Point out each Plasmodium parasite and classify it by life-cycle stage.
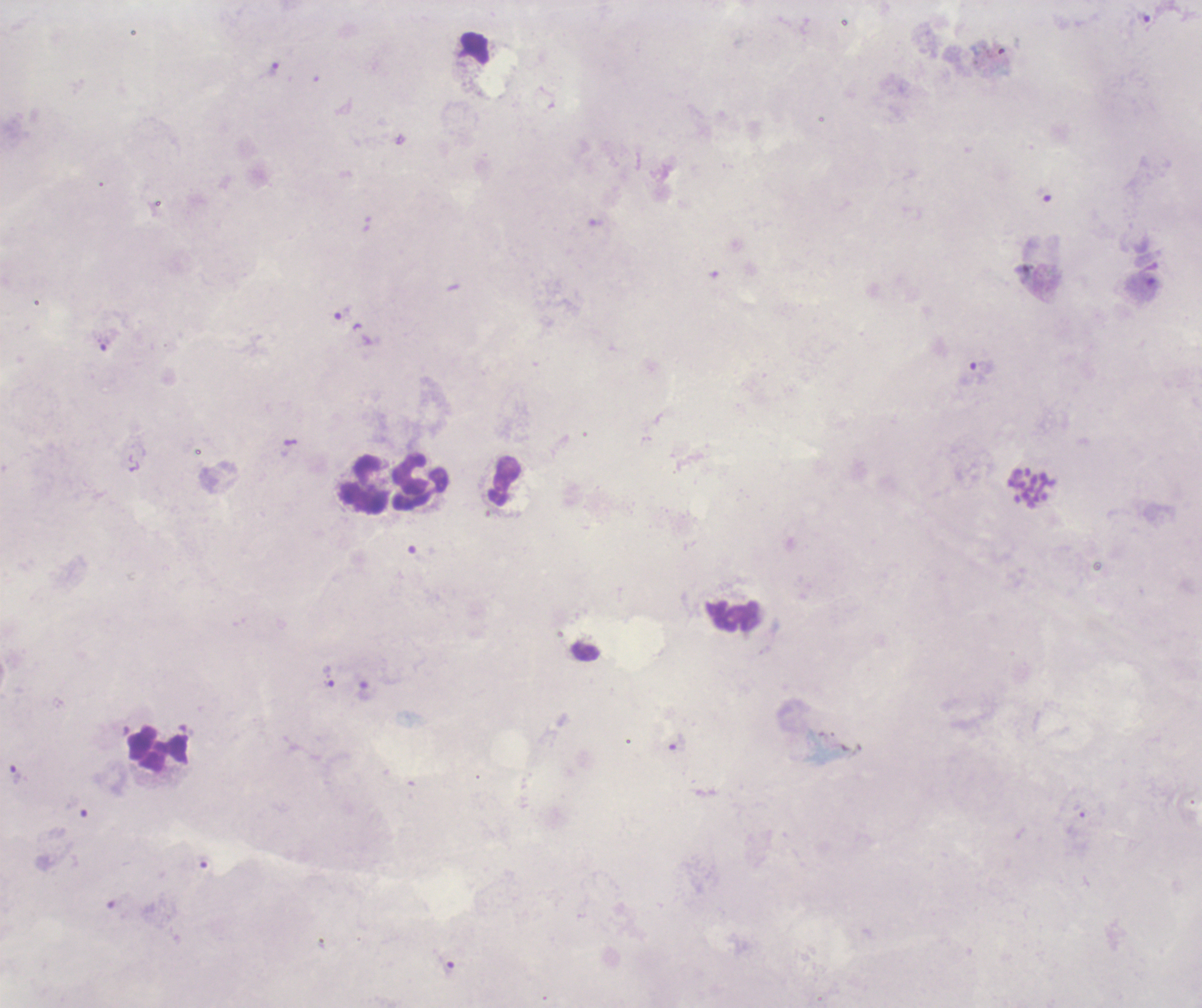
Approximate centers as {x, y} in pixels.
Trophozoites: {1144, 20}, {272, 70}, {342, 313}, {105, 344}, {979, 370}, {330, 681}, {365, 693}, {678, 742}, {16, 775}, {447, 965}.
Schizonts: {1032, 487}.
No gametocyte forms observed.

Approximate centers as {x, y} in pixels.
Summary:
  - Leukocyte locations: {505, 482}, {365, 483}, {420, 483}, {733, 614}, {158, 748}
  - Preparation: thick blood smear
  - Stain: Romanowsky
  - Image size: 1202×1008 pixels
  - Field of view: one from this slide
  - Magnification: 100x
  - Context: previously used in a real diagnosis
  - Coloration quality: bad
  - Background quality: poor